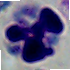
Summary:
  - Magnification: 1000x
  - Modality: micrograph
  - Identification: white blood cell